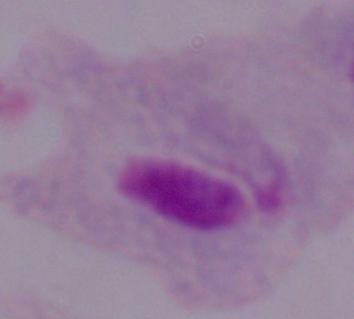
Photomicrograph. 1000x magnification. A trichomonad is shown.